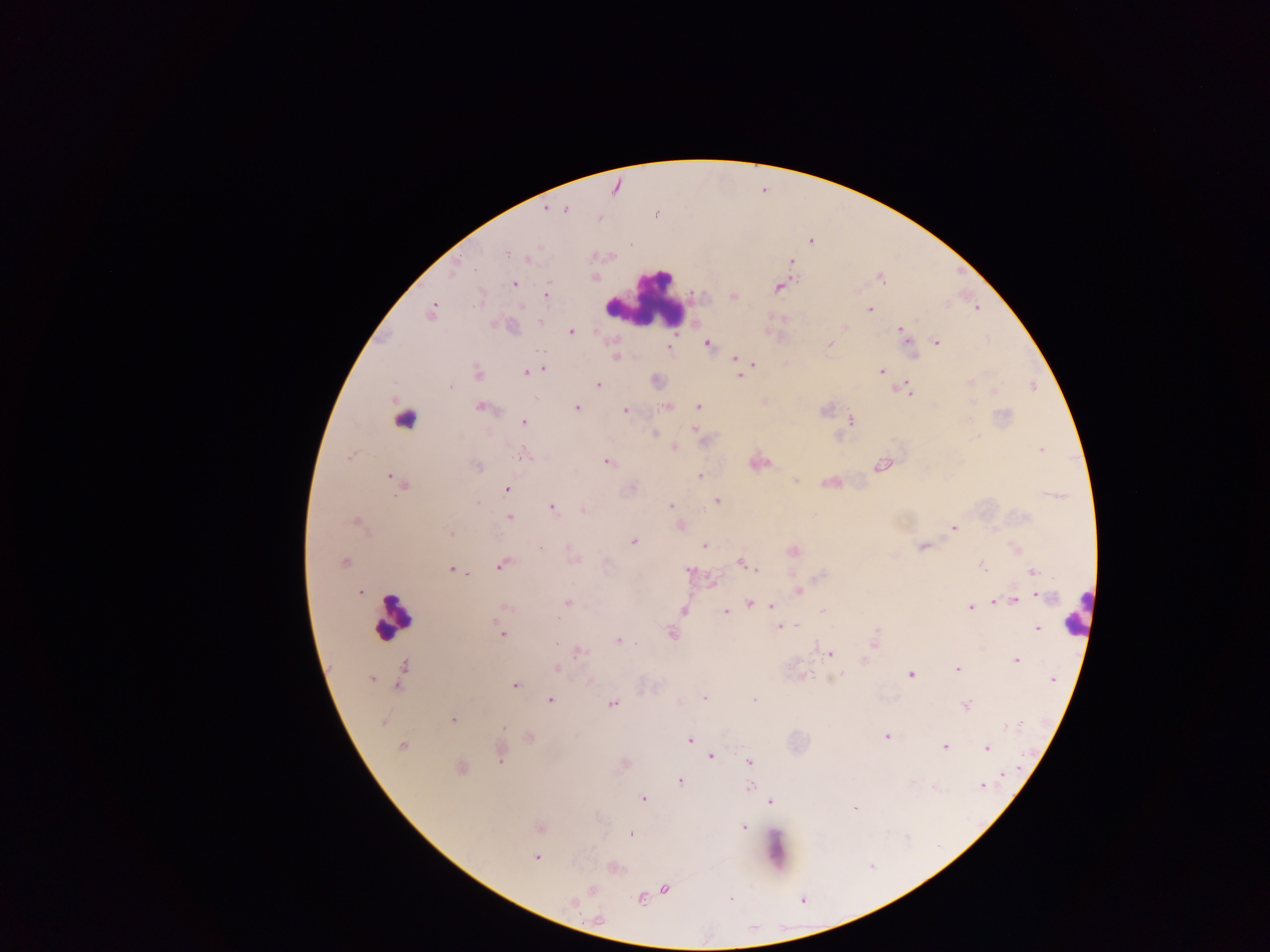
Approximate centers as {x, y} in pixels.
Summary:
  - Leukocyte locations: {646, 297}, {1077, 612}, {393, 617}, {775, 849}
  - Object labeled both malaria parasite and leukocyte by the source: {404, 417}
  - Malaria parasite locations: {545, 208}, {566, 209}, {811, 241}, {505, 254}, {528, 258}, {790, 260}, {456, 263}, {594, 276}, {880, 277}, {513, 283}, {778, 286}, {545, 296}, {732, 296}, {977, 308}, {869, 310}, {432, 311}, {538, 321}, {845, 326}, {900, 329}, {570, 331}, {936, 342}, {829, 343}, {706, 344}, {670, 346}, {913, 354}, {616, 356}, {735, 359}, {751, 363}, {543, 369}, {533, 371}, {882, 371}, {526, 372}, {478, 373}, {740, 375}, {655, 380}, {971, 381}, {598, 384}, {449, 386}, {904, 389}, {994, 392}, {764, 401}, {667, 406}, {481, 407}, {576, 407}, {698, 407}, {625, 409}, {850, 421}, {523, 422}, {696, 431}, {654, 433}, {674, 447}, {1042, 449}, {523, 455}, {607, 461}, {758, 462}, {882, 465}, {476, 466}, {700, 475}, {391, 477}, {796, 480}, {831, 482}, {400, 483}, {505, 488}, {717, 501}, {478, 503}, {670, 505}, {551, 506}, {582, 510}, {509, 517}, {356, 522}, {679, 525}, {953, 528}, {450, 532}, {633, 542}, {704, 546}, {922, 546}, {1016, 549}, {792, 552}, {572, 558}, {344, 561}, {741, 562}, {502, 563}, {982, 565}, {451, 569}, {689, 569}, {757, 570}, {1031, 572}, {467, 574}, {712, 581}, {798, 590}, {360, 592}, {1038, 594}, {1013, 598}, {994, 601}, {749, 602}, {568, 603}, {773, 605}, {505, 607}, {970, 607}, {682, 609}, {726, 612}, {822, 612}, {797, 625}, {780, 627}, {1037, 628}, {502, 633}, {671, 634}, {617, 640}, {874, 641}, {577, 650}, {829, 654}, {1015, 660}, {862, 661}, {557, 668}, {957, 669}, {403, 674}, {839, 674}, {910, 674}, {800, 676}, {371, 678}, {591, 678}, {1052, 679}, {515, 685}, {704, 698}, {754, 699}, {550, 700}, {613, 703}, {966, 705}, {453, 720}, {382, 722}, {503, 727}, {887, 735}, {528, 737}, {688, 740}, {402, 746}, {945, 746}, {987, 748}, {500, 753}, {710, 756}, {749, 762}, {460, 768}, {1003, 774}, {679, 780}, {982, 786}, {935, 787}, {749, 788}, {643, 798}, {769, 802}, {853, 807}, {538, 827}, {742, 827}, {629, 834}, {536, 858}, {614, 867}, {664, 888}, {591, 890}, {731, 898}, {639, 899}, {572, 901}, {598, 919}
  - Preparation: thick blood film
  - Country: Ghana
  - Image size: 1270×952 pixels
  - Field of view: single
  - Capture: mobile-phone photograph through a microscope